Name the parasite shown.
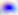

This is Toxoplasma gondii.

modality = photomicrograph
magnification = 400x